Look for Plasmodium parasites.
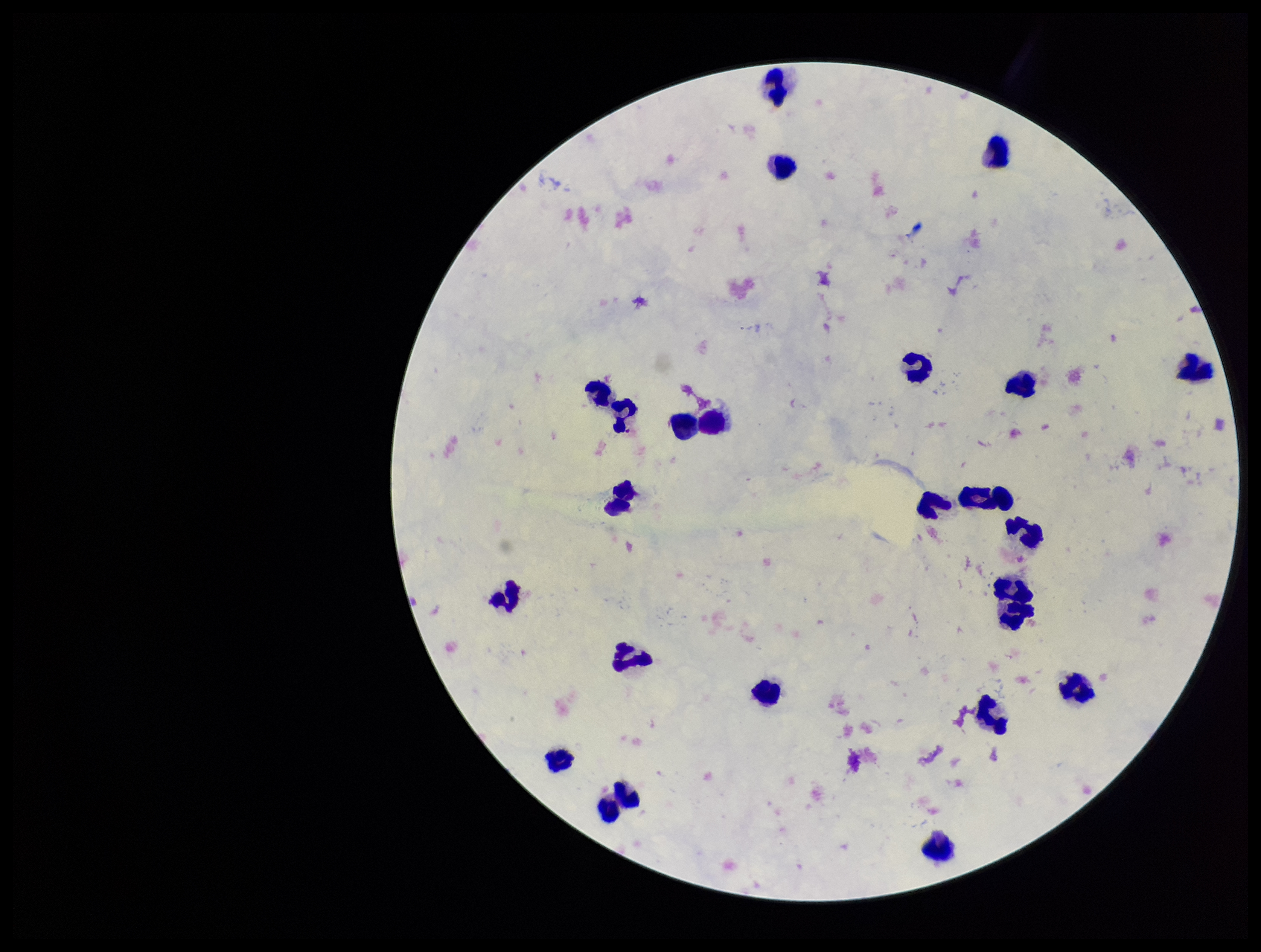
None detected.

Patient malaria status: negative. Image is 1261×952 pixels. Photographed through the microscope eyepiece with a smartphone camera. Preparation: thick. Leukocyte count: 25. Giemsa stain. Parasite count: 0. One field from this slide.